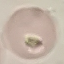
Summary:
  - Malaria status: uninfected
  - Capture: smartphone through the microscope eyepiece
  - Image type: automatically extracted cell patch, resized to 64 × 64 pixels
  - Preparation: thin blood film
  - Stain: Giemsa